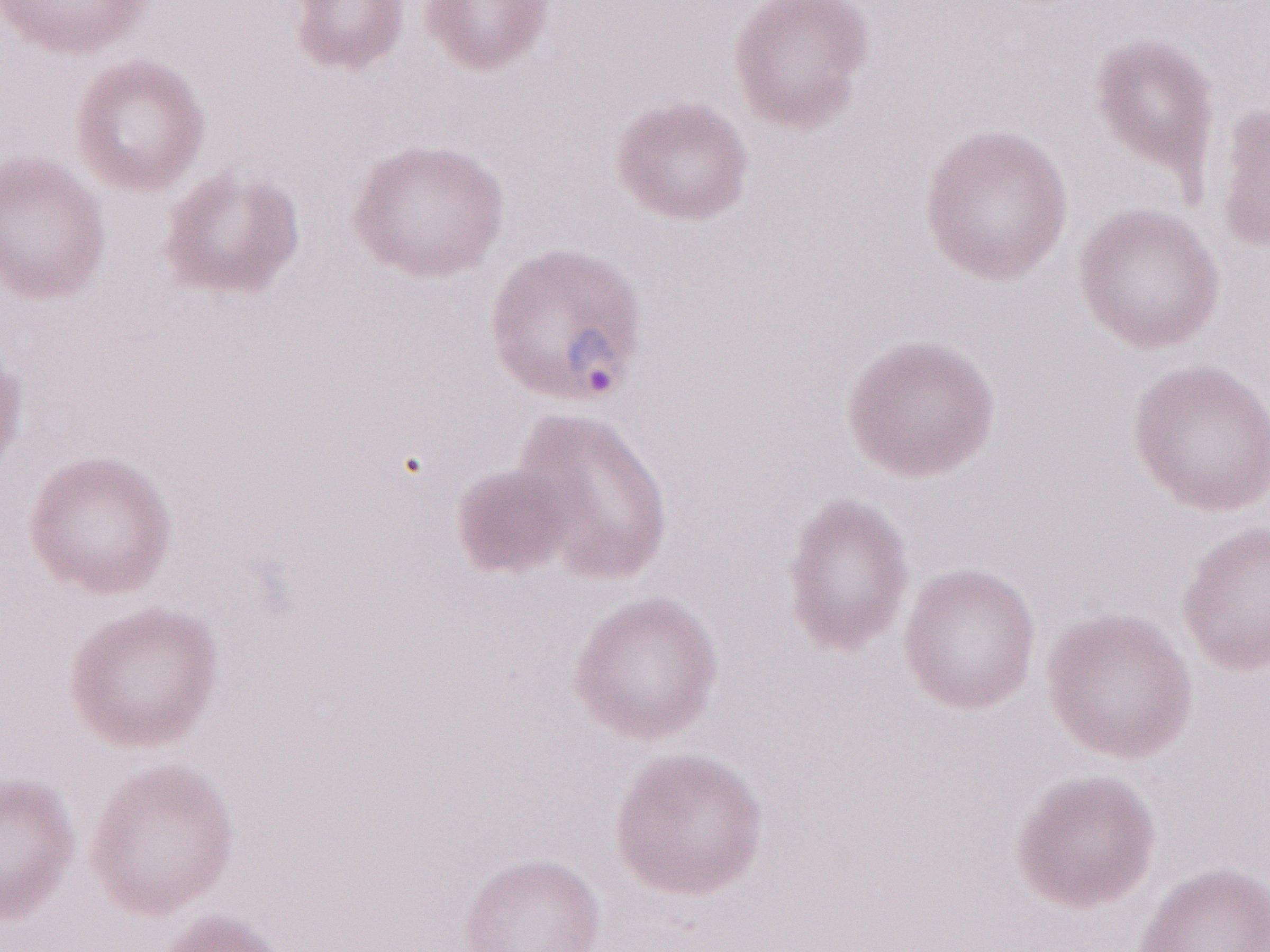 Thin peripheral-blood smear. Olympus BX43 microscope, Olympus DP73 camera. May-Grünwald-Giemsa (MGG) stain. Single field of view. Magnification: 1,000x. Image is 1270×952 pixels. Patient-level malaria diagnosis: positive.